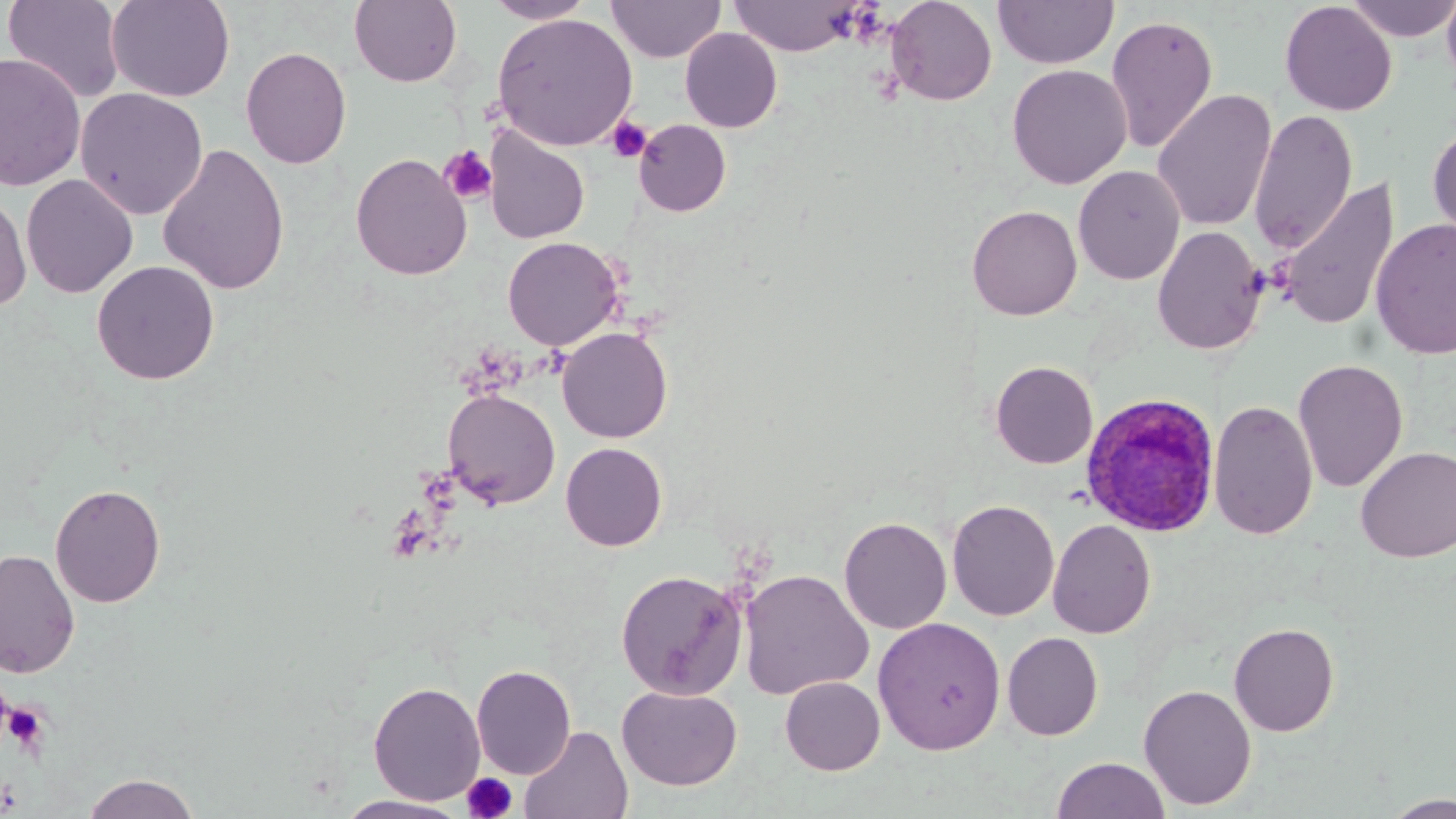 Approximate bounding boxes as (x1,y1)-(x2,y2) corner pairs in pixels. Uninfected red blood cell locations: (2,0)-(126,103), (106,0)-(235,102), (349,0)-(462,87), (483,0)-(596,24), (606,0)-(726,63), (886,0)-(997,106), (993,0)-(1118,69), (1344,0)-(1456,42), (1440,0)-(1456,97), (728,1)-(866,56), (1279,1)-(1397,116), (492,13)-(638,150), (1105,13)-(1219,154), (680,28)-(783,132), (240,46)-(351,169), (0,52)-(86,192), (1007,64)-(1131,189), (75,88)-(208,220), (1152,88)-(1277,232), (1249,109)-(1359,253), (633,119)-(731,217), (1427,122)-(1456,242), (483,127)-(590,244), (157,142)-(290,295), (350,153)-(472,280), (1073,165)-(1186,285), (21,174)-(139,298), (1278,178)-(1399,333), (0,188)-(32,311), (967,205)-(1082,320), (1370,218)-(1456,359), (1152,225)-(1267,355), (502,236)-(624,351), (92,260)-(220,385), (557,327)-(672,443), (1293,358)-(1408,492), (990,360)-(1098,469), (442,388)-(561,508), (1208,399)-(1318,540), (560,442)-(667,551), (1355,446)-(1456,562), (49,482)-(166,608), (947,499)-(1060,621), (838,516)-(951,634), (1047,518)-(1156,638), (0,549)-(80,679), (615,568)-(748,700), (738,568)-(874,700), (872,617)-(1007,756), (1228,622)-(1340,736), (1002,632)-(1104,740), (471,664)-(576,779), (780,676)-(885,775), (368,680)-(485,805), (1138,683)-(1257,810), (617,685)-(743,790), (519,726)-(633,819), (1051,756)-(1171,818), (80,772)-(202,818), (1382,794)-(1456,818), (334,795)-(471,818). Plasmodium ovale-infected red blood cell locations: (1079,390)-(1223,542). Platelet locations: (606,117)-(652,163), (439,145)-(498,205), (4,700)-(51,754), (462,772)-(518,819). Slide-level diagnosis: Plasmodium ovale. Optical microscopy. May-Grünwald-Giemsa stain. Image is 1456×819 pixels. Single field of view. 1000x magnification. Thin blood film.